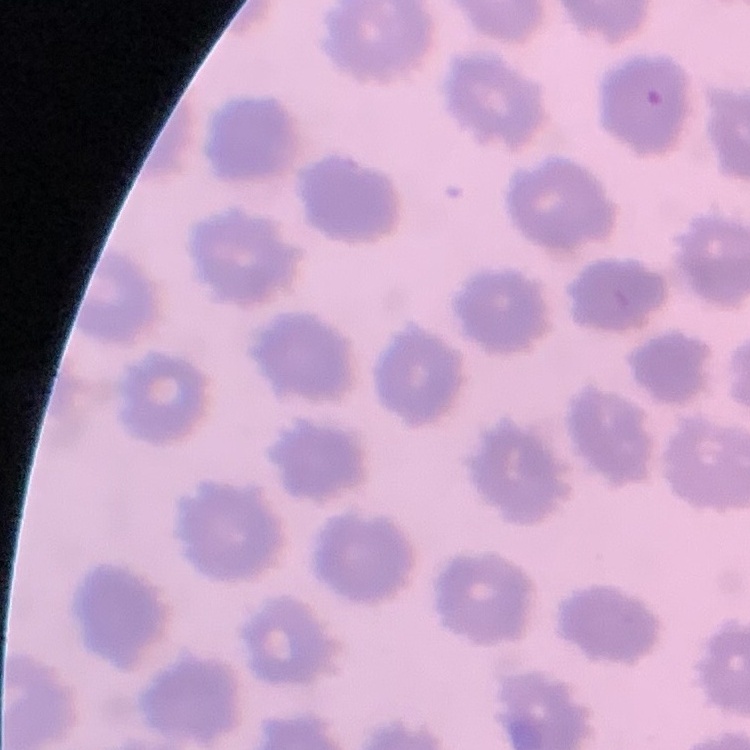

The erythrocytes show no rouleaux formation. Thin peripheral smear. Stained with either Field's or Giemsa. Square crop of a larger photomicrograph.